Point out each leukocyte.
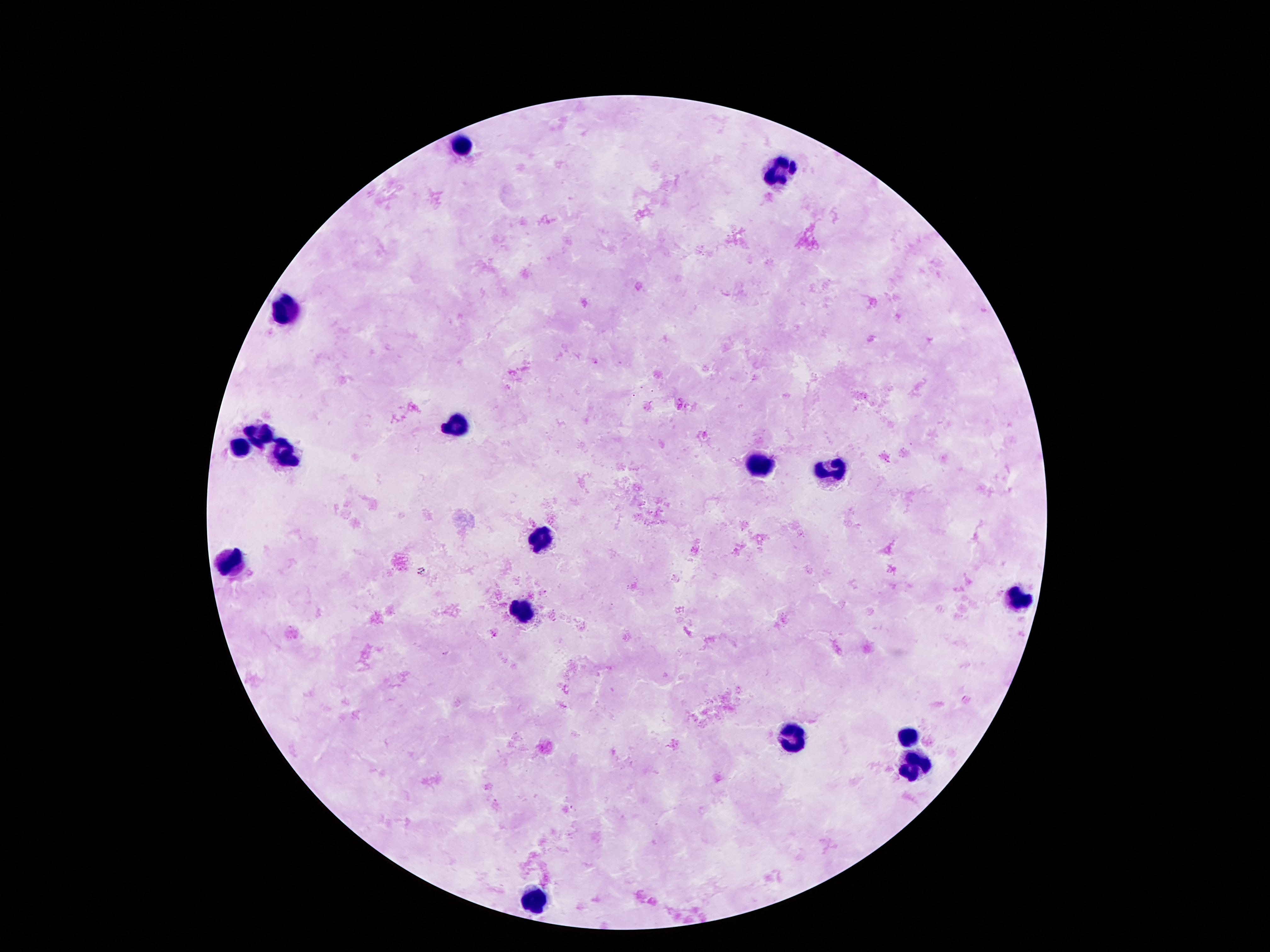
Approximate centers as [x, y] in pixels.
Leukocytes: [461, 148], [782, 170], [287, 312], [457, 427], [260, 434], [237, 445], [285, 454], [761, 466], [829, 471], [541, 537], [234, 559], [1015, 602], [523, 609], [795, 736], [908, 736], [917, 767], [530, 900].

{
  "capture": "smartphone camera through the microscope eyepiece",
  "patient_malaria_status": "uninfected",
  "preparation": "thick blood smear",
  "field_of_view": "single",
  "stain": "Giemsa",
  "image_size": "1270×952 pixels",
  "magnification": "100x"
}